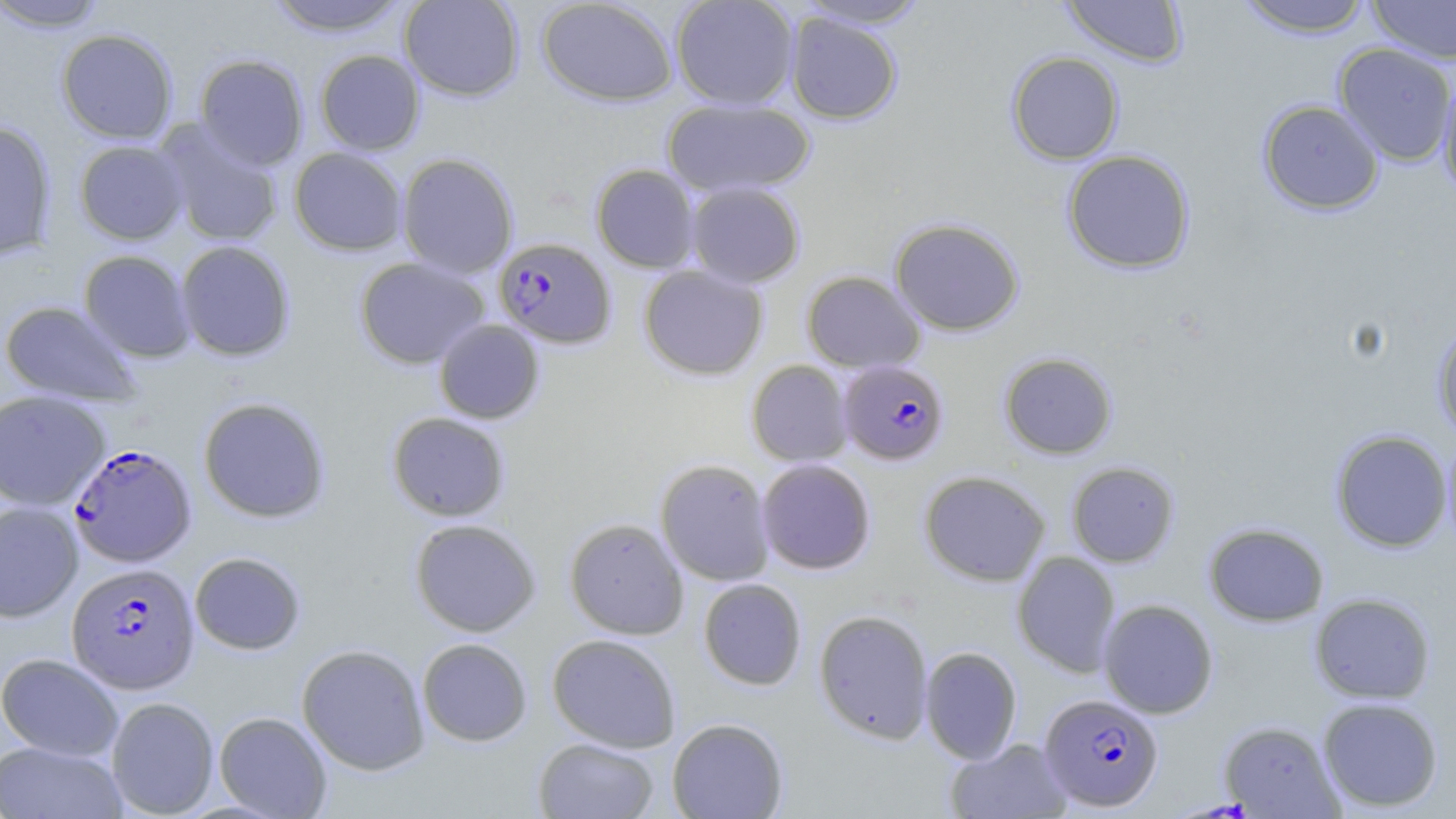
slide-level diagnosis = Plasmodium falciparum
magnification = 1000x
preparation = thin blood smear
stain = May-Grünwald-Giemsa
Plasmodium falciparum-infected red blood cell locations = approximate bounding boxes as (x1, y1, x2, y2) in pixels: (493, 237, 616, 349), (838, 360, 950, 465), (68, 443, 197, 567), (66, 563, 200, 694), (1039, 693, 1163, 811)
image size = 1456×819 pixels
field of view = single
uninfected red blood cell locations = approximate bounding boxes as (x1, y1, x2, y2) in pixels: (263, 0, 412, 37), (399, 0, 525, 101), (537, 0, 678, 106), (670, 0, 799, 110), (794, 0, 931, 29), (1060, 0, 1189, 68), (1234, 0, 1375, 38), (1367, 0, 1456, 64), (1, 1, 109, 32), (785, 12, 903, 125), (56, 29, 178, 144), (1333, 43, 1456, 166), (314, 49, 425, 155), (1006, 51, 1124, 165), (194, 54, 309, 171), (1438, 69, 1456, 200), (662, 97, 815, 198), (1257, 99, 1384, 215), (0, 120, 57, 260), (155, 120, 284, 248), (74, 140, 189, 245), (289, 147, 408, 256), (1061, 149, 1195, 274), (397, 152, 519, 278), (591, 164, 700, 272), (685, 181, 805, 287), (890, 217, 1024, 336), (176, 240, 295, 362), (78, 250, 195, 363), (354, 257, 490, 369), (638, 265, 769, 380), (801, 270, 925, 373), (0, 301, 143, 407), (433, 319, 545, 424), (1432, 321, 1456, 441), (998, 351, 1118, 459), (746, 360, 852, 466), (0, 389, 110, 511), (197, 396, 332, 523), (386, 412, 511, 522), (1330, 429, 1452, 552), (1442, 431, 1456, 551), (655, 458, 775, 586), (756, 458, 876, 575), (1066, 461, 1179, 567), (919, 470, 1051, 586), (0, 501, 83, 622), (564, 517, 690, 639), (409, 518, 541, 637), (1203, 522, 1329, 627), (189, 551, 306, 655), (1011, 551, 1121, 678), (698, 578, 807, 690), (1309, 592, 1436, 704), (1098, 599, 1218, 718), (814, 609, 934, 744), (547, 633, 681, 753), (417, 638, 532, 746), (296, 643, 430, 775), (920, 646, 1022, 764), (0, 653, 123, 761), (106, 697, 219, 817), (1317, 697, 1443, 812), (214, 711, 333, 818), (667, 717, 788, 819), (1219, 720, 1343, 818), (533, 738, 659, 819), (945, 738, 1073, 819), (0, 741, 127, 819)
modality = optical microscopy